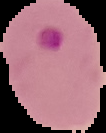
{
  "image_size": "106×133 pixels",
  "preparation": "thin blood film",
  "malaria_status": "parasitized",
  "image_type": "cell region segmented out of the field of view; surrounding area masked to black"
}